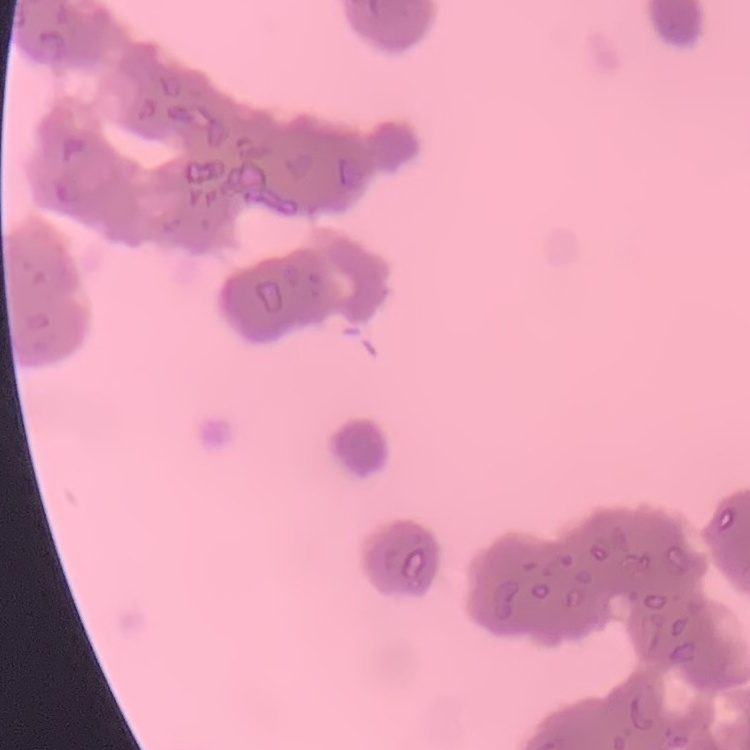

The red blood cells exhibit rouleaux formation. Field's or Giemsa stain. Thin blood film. Square crop of a larger photomicrograph.